Assess the morphology of the red blood cells.
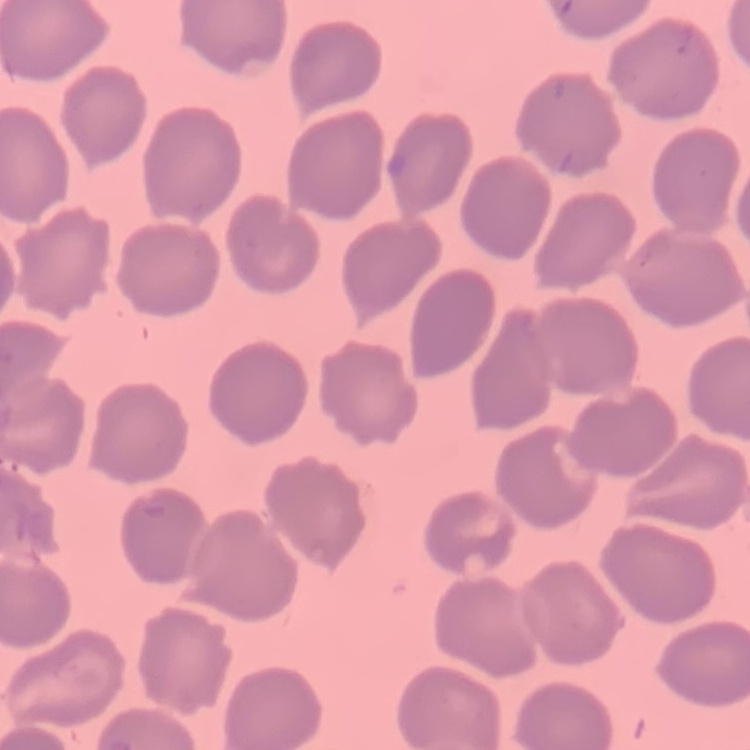
No rouleaux formation.

Summary:
  - Preparation: thin blood smear
  - Stain: Field's or Giemsa
  - Image type: one tile cut from a larger photomicrograph